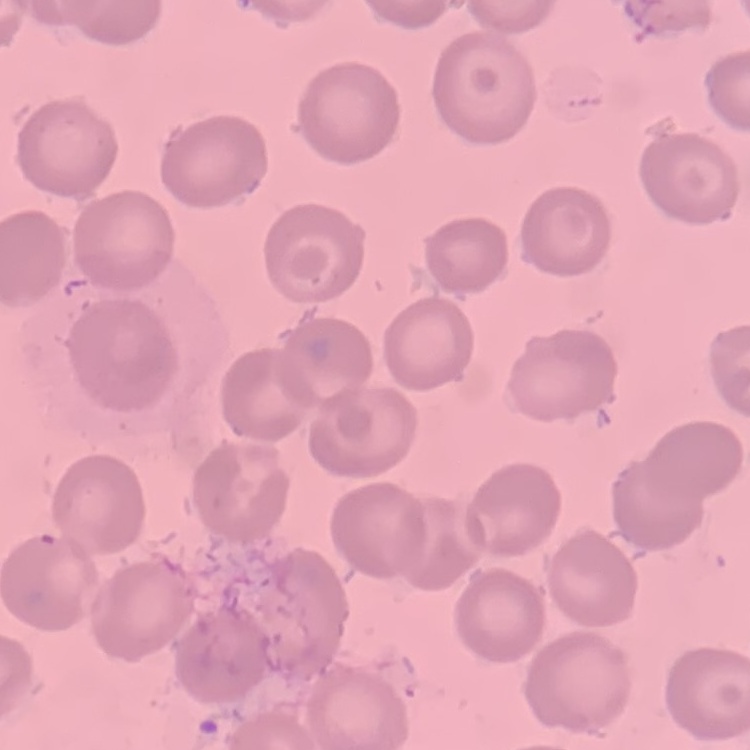 The erythrocytes show no rouleaux formation. Thin blood film. One tile cut from a larger photomicrograph. Stained with either Field's or Giemsa.